Name the parasite shown.
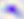

Toxoplasma gondii.

modality = photomicrograph
magnification = 400x